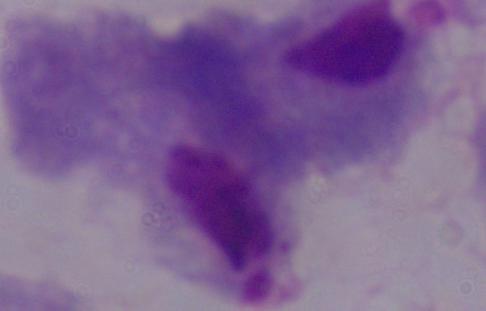
Summary:
  - Magnification: 1000x
  - Identification: trichomonad
  - Modality: micrograph